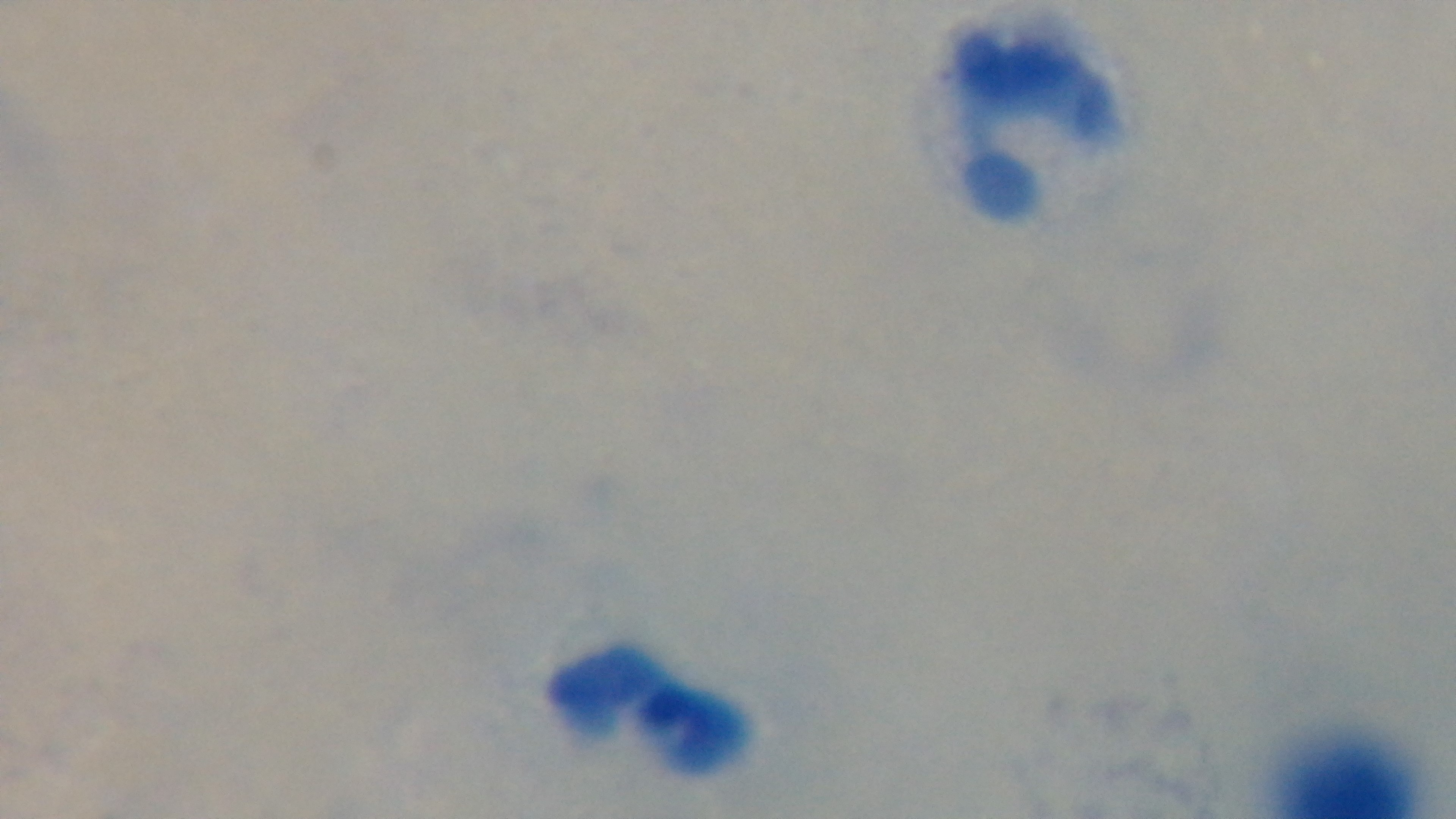

field_of_view: one from the slide
stain: Giemsa
preparation: thick smear
objective: 100x oil immersion
malaria_status: uninfected
modality: light microscopy
capture: mounted 4K digital camera